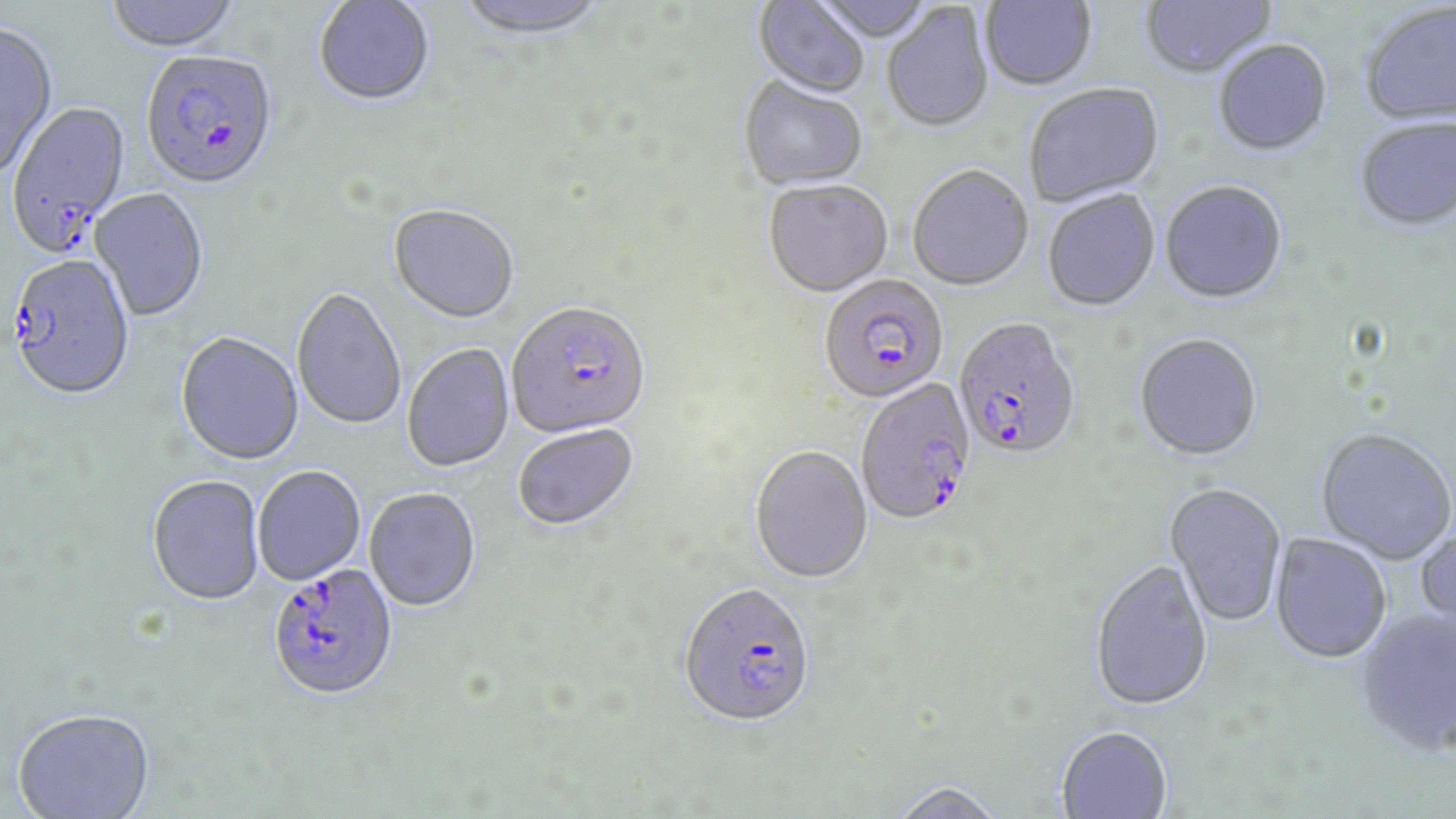 Approximate bounding boxes as (x1,y1)-(x2,y2) corner pairs in pixels. Plasmodium falciparum-infected red blood cell locations: (141,53)-(279,194), (5,101)-(132,259), (6,256)-(135,403), (818,277)-(949,407), (507,305)-(651,441), (952,320)-(1082,464), (855,378)-(979,529), (268,566)-(399,705), (679,587)-(816,732). Uninfected red blood cell locations: (106,0)-(242,55), (455,0)-(609,43), (809,0)-(938,44), (980,0)-(1097,92), (1140,0)-(1276,82), (313,1)-(435,109), (752,1)-(870,101), (881,5)-(994,135), (1361,5)-(1456,128), (0,25)-(59,184), (1213,42)-(1333,158), (738,79)-(868,193), (1024,84)-(1165,209), (1355,119)-(1456,233), (908,167)-(1033,293), (764,182)-(893,299), (1160,183)-(1288,306), (88,188)-(208,323), (1043,191)-(1161,314), (387,205)-(519,326), (291,290)-(406,432), (176,333)-(304,468), (1134,335)-(1263,464), (402,344)-(515,474), (513,426)-(640,534), (1316,430)-(1455,566), (749,447)-(873,587), (253,467)-(366,586), (147,477)-(265,608), (1164,484)-(1286,629), (365,490)-(480,613), (1414,528)-(1456,639), (1270,533)-(1392,666), (1089,562)-(1213,715), (1356,610)-(1455,759), (13,712)-(156,819), (1056,728)-(1173,818), (887,784)-(1007,819). Slide-level diagnosis: Plasmodium falciparum. Optical microscopy. Thin blood film. May-Grünwald-Giemsa stain. Captured at 1000x magnification. Image is 1456×819 pixels. Single field of view.